Describe the morphology of the red blood cells.
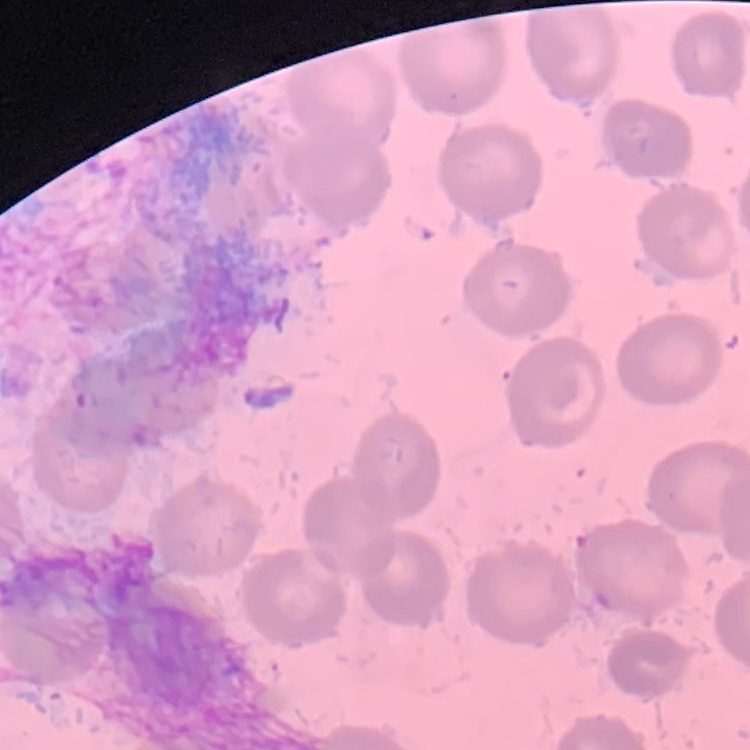
No rouleaux formation.

Summary:
  - Preparation: thin peripheral smear
  - Image type: square crop of a larger photomicrograph
  - Stain: Field's or Giemsa